Classify this cell by malaria status.
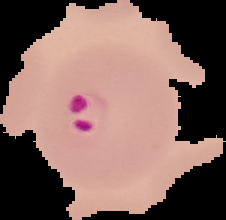

Parasitized.

Summary:
  - Image type: cell region segmented out of the field of view; surrounding area masked to black
  - Image size: 226×220 pixels
  - Preparation: thin blood film